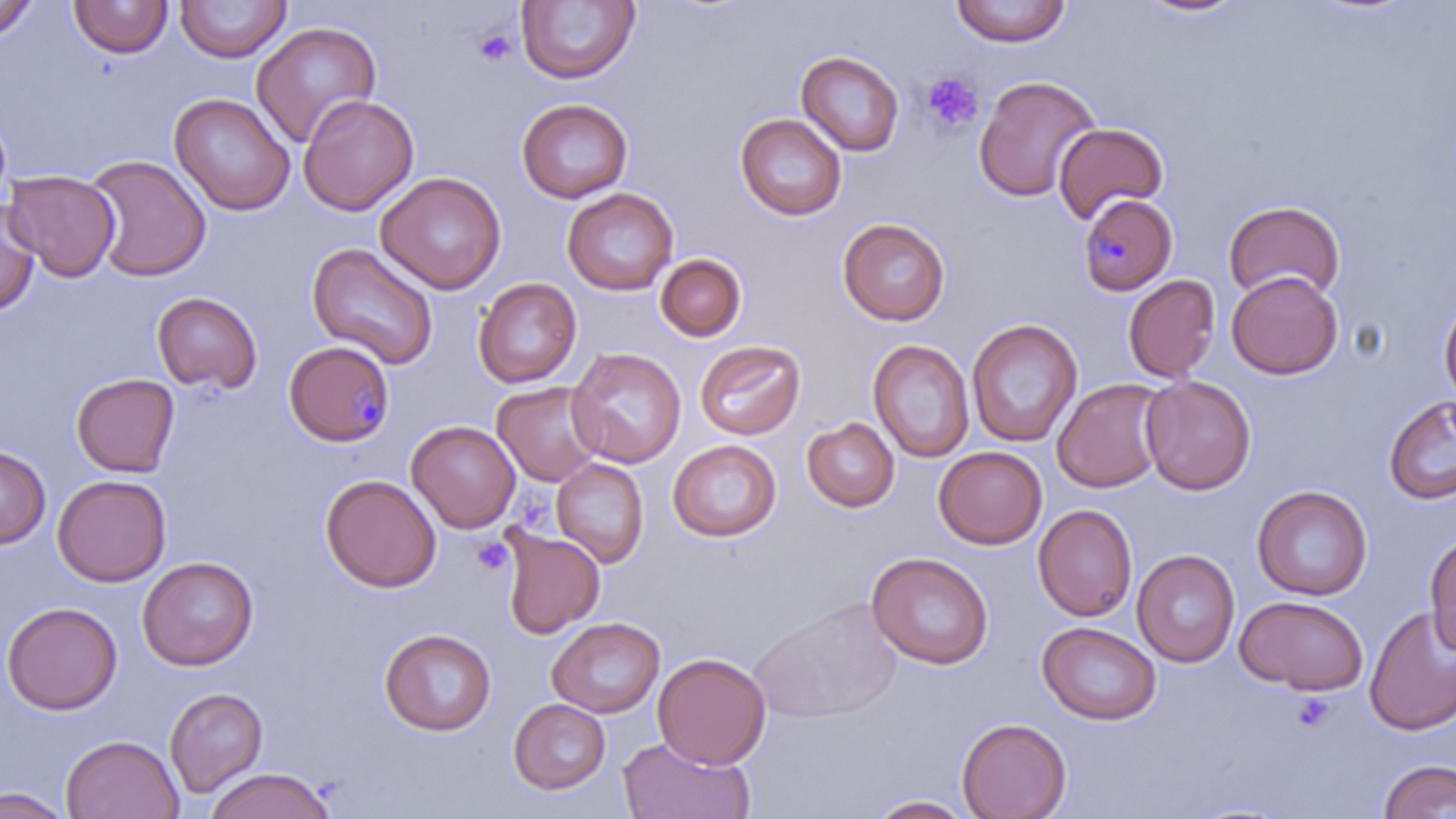
{
  "slide_level_diagnosis": "Plasmodium malariae",
  "image_size": "1456×819 pixels",
  "platelet_locations": "approximate bounding boxes as (x1, y1, x2, y2) in pixels: (473, 27, 517, 67), (921, 71, 984, 132), (472, 536, 514, 577), (1289, 691, 1337, 732)",
  "uninfected_red_blood_cell_locations": "approximate bounding boxes as (x1, y1, x2, y2) in pixels: (0, 0, 40, 40), (68, 0, 173, 59), (176, 0, 290, 62), (950, 0, 1072, 47), (1133, 0, 1250, 19), (515, 1, 640, 85), (250, 21, 382, 148), (795, 50, 905, 156), (973, 74, 1101, 202), (169, 93, 295, 215), (298, 94, 418, 216), (516, 98, 633, 203), (735, 113, 847, 220), (1053, 122, 1168, 224), (84, 154, 211, 282), (2, 170, 121, 281), (375, 172, 506, 294), (562, 187, 678, 295), (0, 195, 40, 316), (1223, 199, 1346, 302), (837, 217, 950, 326), (306, 242, 439, 369), (655, 253, 747, 341), (1227, 271, 1343, 379), (1123, 274, 1221, 383), (472, 278, 582, 388), (151, 291, 261, 393), (1439, 294, 1456, 408), (966, 319, 1083, 449), (868, 339, 974, 463), (694, 340, 806, 441), (566, 347, 686, 468), (70, 372, 180, 477), (1140, 375, 1256, 495), (1052, 378, 1169, 493), (492, 381, 605, 486), (1384, 395, 1456, 505), (801, 417, 899, 512), (406, 420, 520, 533), (668, 440, 781, 542), (0, 444, 51, 549), (933, 446, 1047, 549), (551, 458, 649, 567), (52, 474, 172, 586), (320, 474, 441, 593), (1252, 485, 1372, 600), (1033, 504, 1137, 622), (499, 529, 605, 639), (1424, 532, 1456, 656), (1132, 549, 1239, 667), (866, 552, 993, 669), (137, 556, 259, 670), (1236, 596, 1368, 694), (748, 598, 903, 724), (1, 602, 122, 715), (1364, 605, 1456, 736), (546, 616, 665, 718), (1037, 621, 1162, 725), (379, 627, 496, 736), (653, 653, 770, 769), (164, 687, 269, 798), (508, 698, 611, 794), (956, 717, 1072, 819), (59, 734, 184, 818), (618, 737, 756, 819), (1378, 759, 1456, 819), (204, 768, 336, 819), (1, 787, 74, 818), (864, 794, 978, 818)",
  "field_of_view": "one of a larger specimen",
  "plasmodium_malariae_infected_red_blood_cell_locations": "approximate bounding boxes as (x1, y1, x2, y2) in pixels: (1077, 194, 1177, 296), (284, 340, 395, 447)",
  "modality": "light microscopy",
  "magnification": "1000x",
  "stain": "May-Grünwald-Giemsa",
  "preparation": "thin blood film"
}